Report the malaria status of this cell.
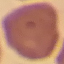

It is uninfected.

Summary:
  - Capture: smartphone camera at the microscope eyepiece
  - Image type: cell patch, automatically extracted from a larger field of view and resized to 64 × 64 pixels
  - Stain: Giemsa
  - Preparation: thin blood smear